Describe the morphology of the erythrocytes.
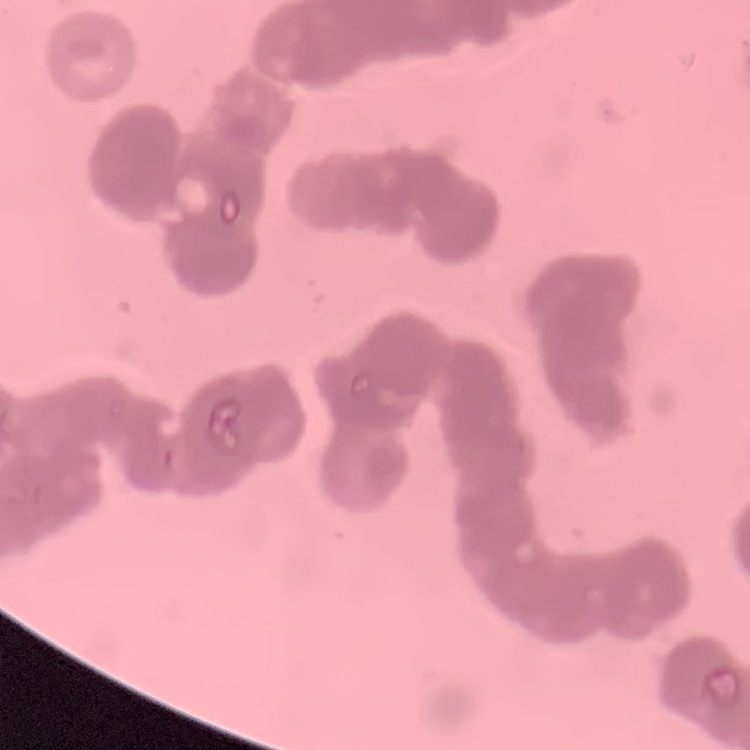

Rouleaux formation.

preparation = thin peripheral smear
stain = Field's or Giemsa
image type = one tile cut from a larger photomicrograph